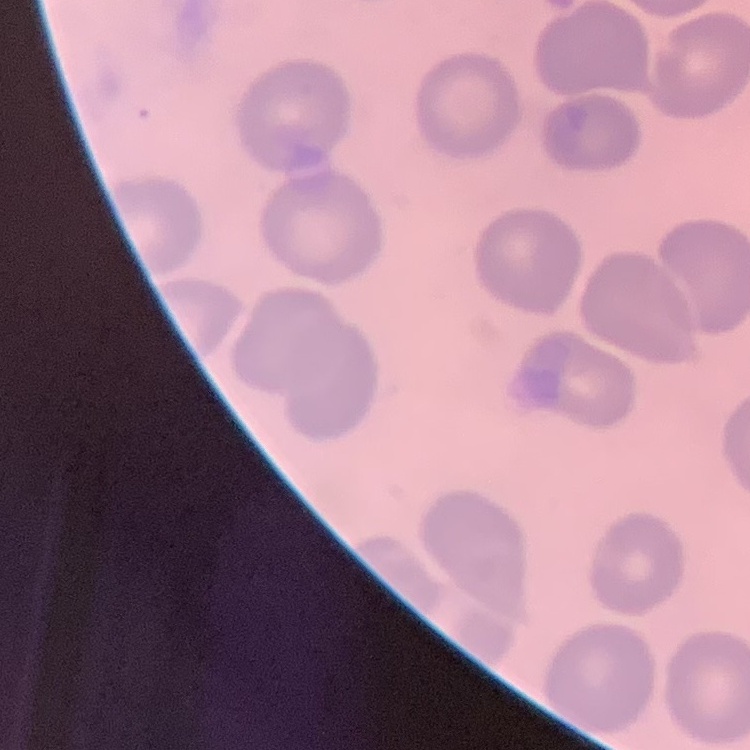
erythrocyte morphology = no rouleaux formation
image type = one tile cut from a larger photomicrograph
preparation = thin blood film
stain = Field's or Giemsa